Identify the parasite.
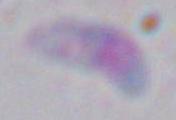

Toxoplasma gondii.

Captured at 1000x magnification. Micrograph.